Look for Plasmodium parasites.
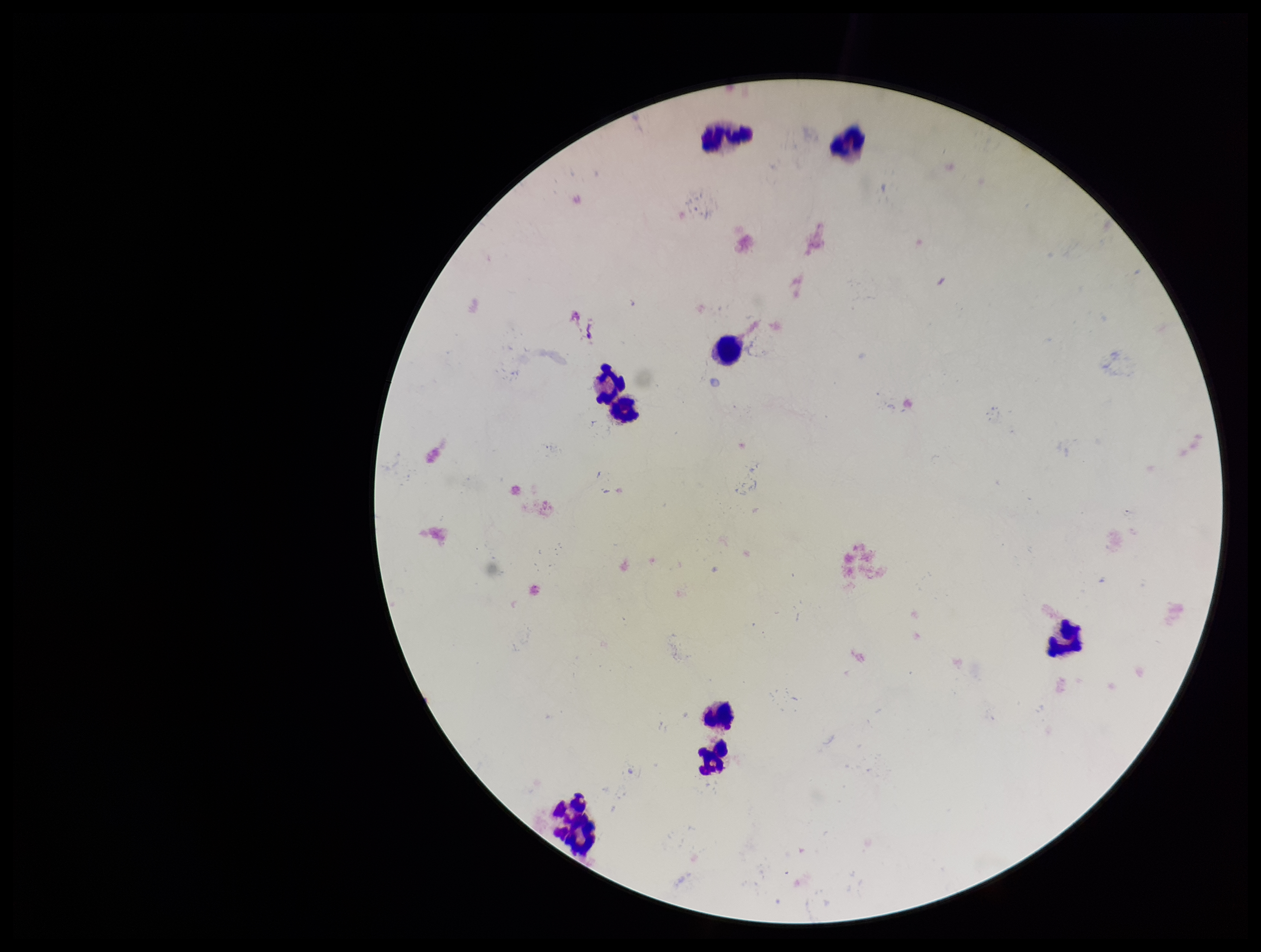
None seen.

Summary:
  - Leukocyte count: 9
  - Field of view: single
  - Preparation: thick blood smear
  - Parasite count: 0
  - Stain: Giemsa
  - Patient malaria status: negative
  - Image size: 1261×952 pixels
  - Capture: smartphone photograph through the microscope eyepiece